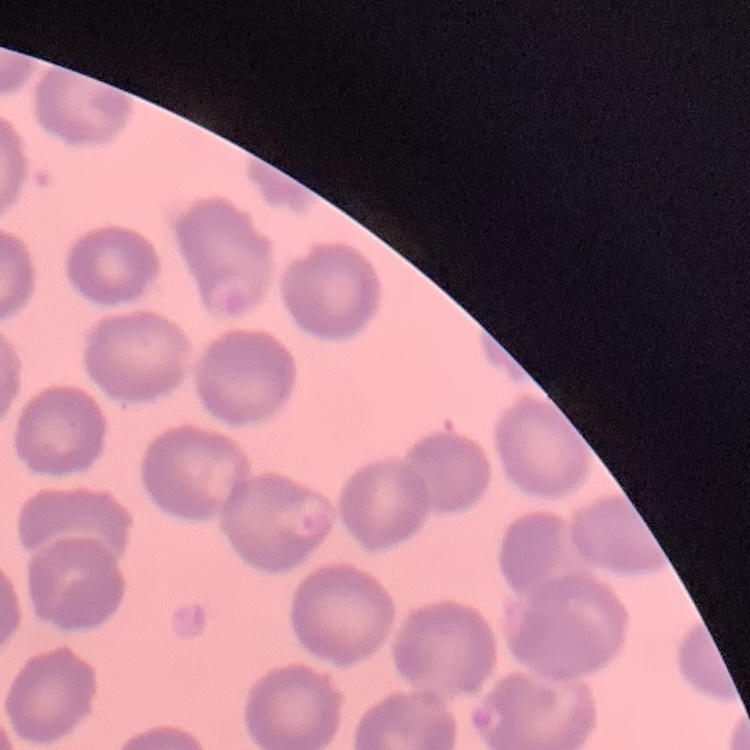

Summary:
  - Red blood cell morphology: no rouleaux formation
  - Stain: Field's or Giemsa
  - Preparation: thin blood film
  - Image type: square crop of a larger photomicrograph